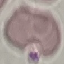
result = no malaria parasites seen
capture = smartphone camera at the microscope eyepiece
preparation = thin smear
stain = Giemsa
image type = automatically extracted cell patch, resized to 64 × 64 pixels